Classify this cell by malaria status.
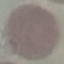
It is uninfected.

preparation = thin blood film
stain = Giemsa
capture = smartphone camera at the microscope eyepiece
image type = automatically extracted cell patch, resized to 64 × 64 pixels